Comment on the morphology of the erythrocytes.
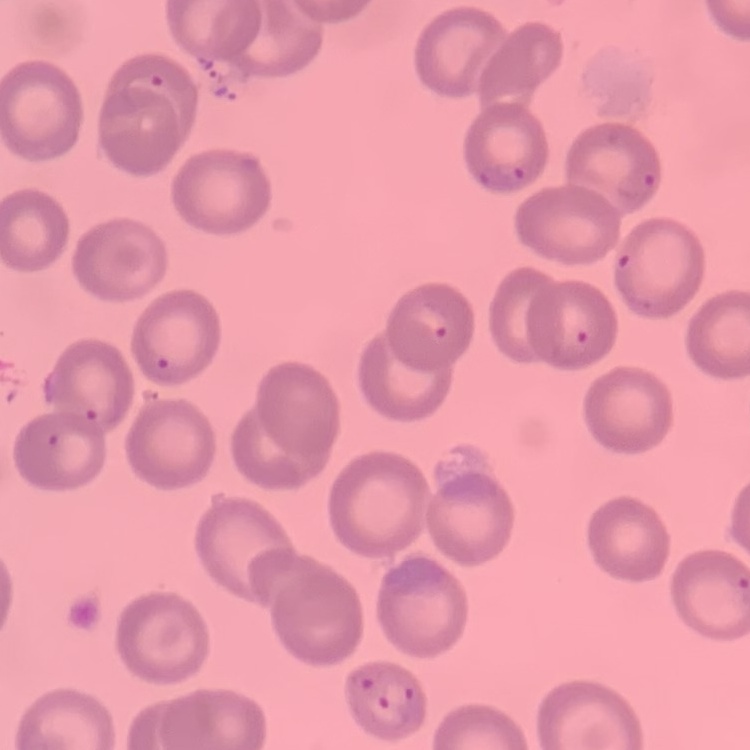

They show no rouleaux formation.

One tile cut from a larger photomicrograph. Field's or Giemsa stain. Thin blood smear.